Assess this cell for malaria.
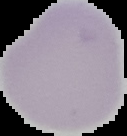

It is uninfected.

image_type: cell region segmented out of the field of view; surrounding area masked to black
preparation: thin blood film
image_size: 127×136 pixels